Classify this cell by malaria status.
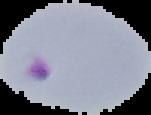

Parasitized.

From a thin blood smear. Segmented cell region on a black background. Image is 151×115 pixels.